Identify the parasite.
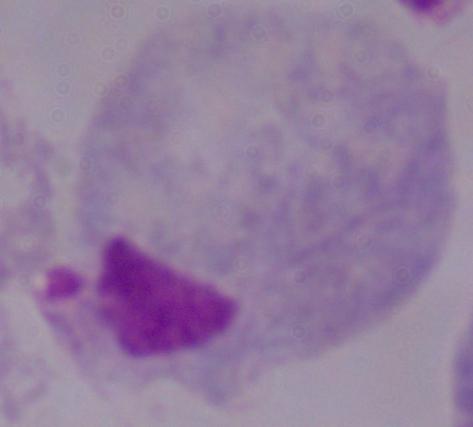
A trichomonad.

Summary:
  - Modality: photomicrograph
  - Magnification: 1000x